Give the extent of all Plasmodium falciparum-infected red blood cells.
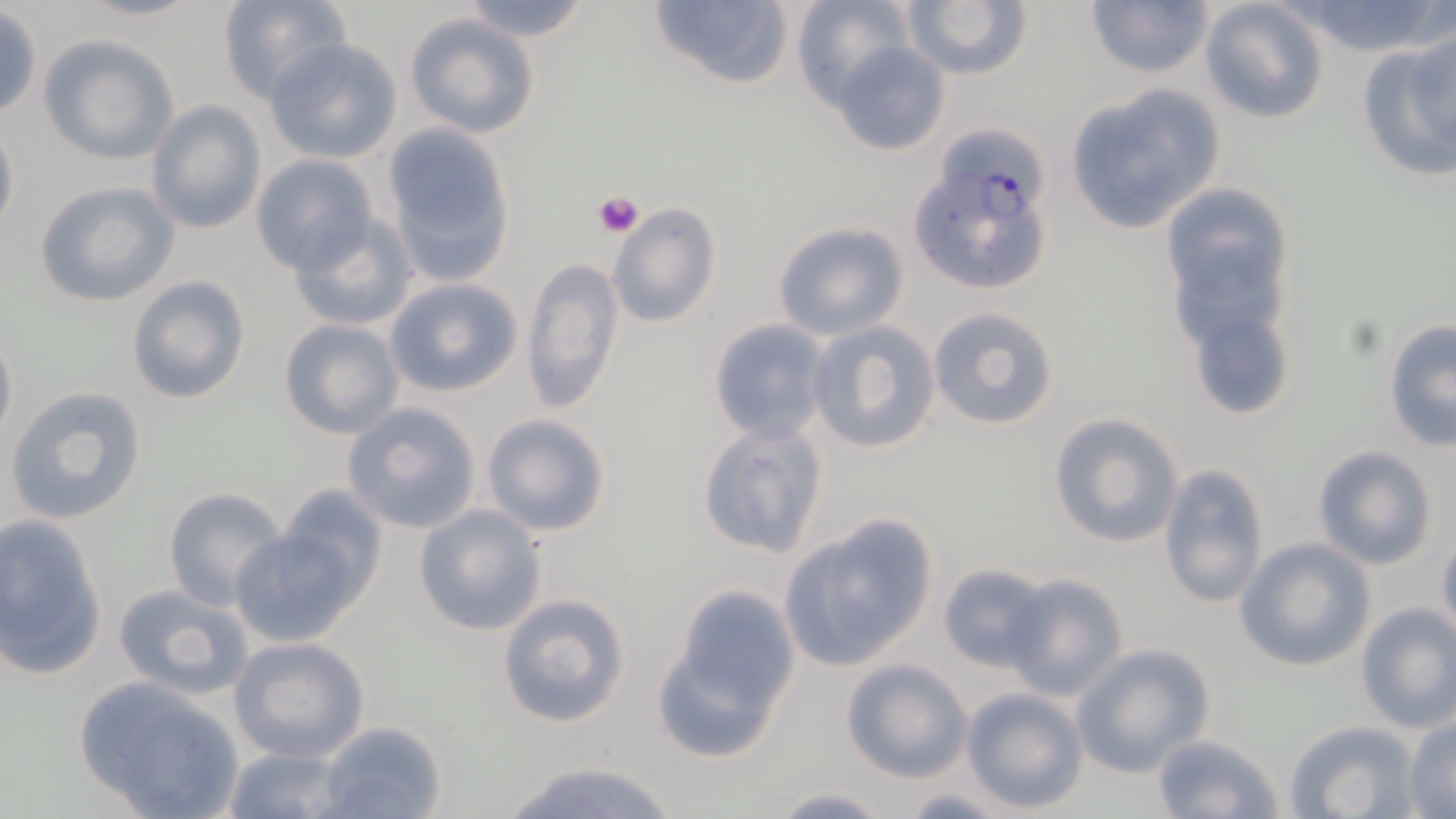

Approximate bounding boxes as (x1, y1, x2, y2) in pixels.
Plasmodium falciparum-infected red blood cells: (908, 149, 1058, 300).

{
  "slide_level_diagnosis": "Plasmodium falciparum",
  "platelet_locations": "approximate bounding boxes as (x1, y1, x2, y2) in pixels: (593, 192, 643, 237)",
  "field_of_view": "one of a larger specimen",
  "uninfected_red_blood_cell_locations": "approximate bounding boxes as (x1, y1, x2, y2) in pixels: (72, 0, 207, 24), (216, 0, 354, 105), (454, 0, 595, 42), (647, 0, 795, 90), (790, 0, 916, 110), (1284, 0, 1456, 61), (900, 1, 1032, 82), (1083, 1, 1215, 82), (1198, 1, 1331, 126), (1, 7, 43, 121), (403, 13, 542, 139), (1406, 26, 1456, 164), (1356, 32, 1456, 185), (39, 34, 179, 165), (264, 38, 403, 163), (830, 41, 951, 158), (1061, 84, 1226, 234), (146, 101, 266, 234), (0, 113, 19, 242), (380, 121, 518, 282), (250, 153, 379, 274), (35, 181, 180, 308), (1159, 186, 1300, 392), (607, 203, 721, 330), (287, 214, 419, 334), (772, 219, 910, 340), (522, 255, 624, 412), (126, 274, 252, 406), (384, 277, 523, 398), (1180, 299, 1299, 421), (926, 306, 1060, 431), (277, 318, 405, 439), (707, 318, 833, 444), (1384, 319, 1455, 451), (807, 321, 941, 455), (0, 324, 18, 454), (5, 385, 149, 526), (342, 402, 483, 533), (480, 412, 616, 539), (1047, 413, 1184, 548), (694, 422, 829, 561), (1311, 446, 1438, 570), (1158, 461, 1271, 610), (278, 484, 390, 600), (162, 487, 288, 609), (413, 505, 548, 637), (1, 514, 107, 679), (778, 516, 937, 670), (228, 528, 363, 649), (1436, 535, 1456, 641), (1234, 537, 1376, 672), (937, 563, 1055, 671), (1002, 572, 1129, 699), (113, 582, 255, 700), (658, 585, 798, 744), (496, 593, 631, 727), (1355, 604, 1456, 735), (228, 636, 371, 762), (1072, 643, 1216, 776), (840, 659, 972, 782), (73, 677, 244, 819), (960, 686, 1089, 813), (1404, 717, 1456, 817), (1285, 720, 1424, 819), (317, 721, 448, 819), (1151, 733, 1283, 818), (221, 746, 353, 818), (488, 754, 688, 819), (766, 786, 896, 818), (897, 788, 1015, 818)",
  "magnification": "1000x",
  "modality": "optical microscopy",
  "image_size": "1456×819 pixels",
  "preparation": "thin blood film",
  "stain": "May-Grünwald-Giemsa"
}